State the preparation type.
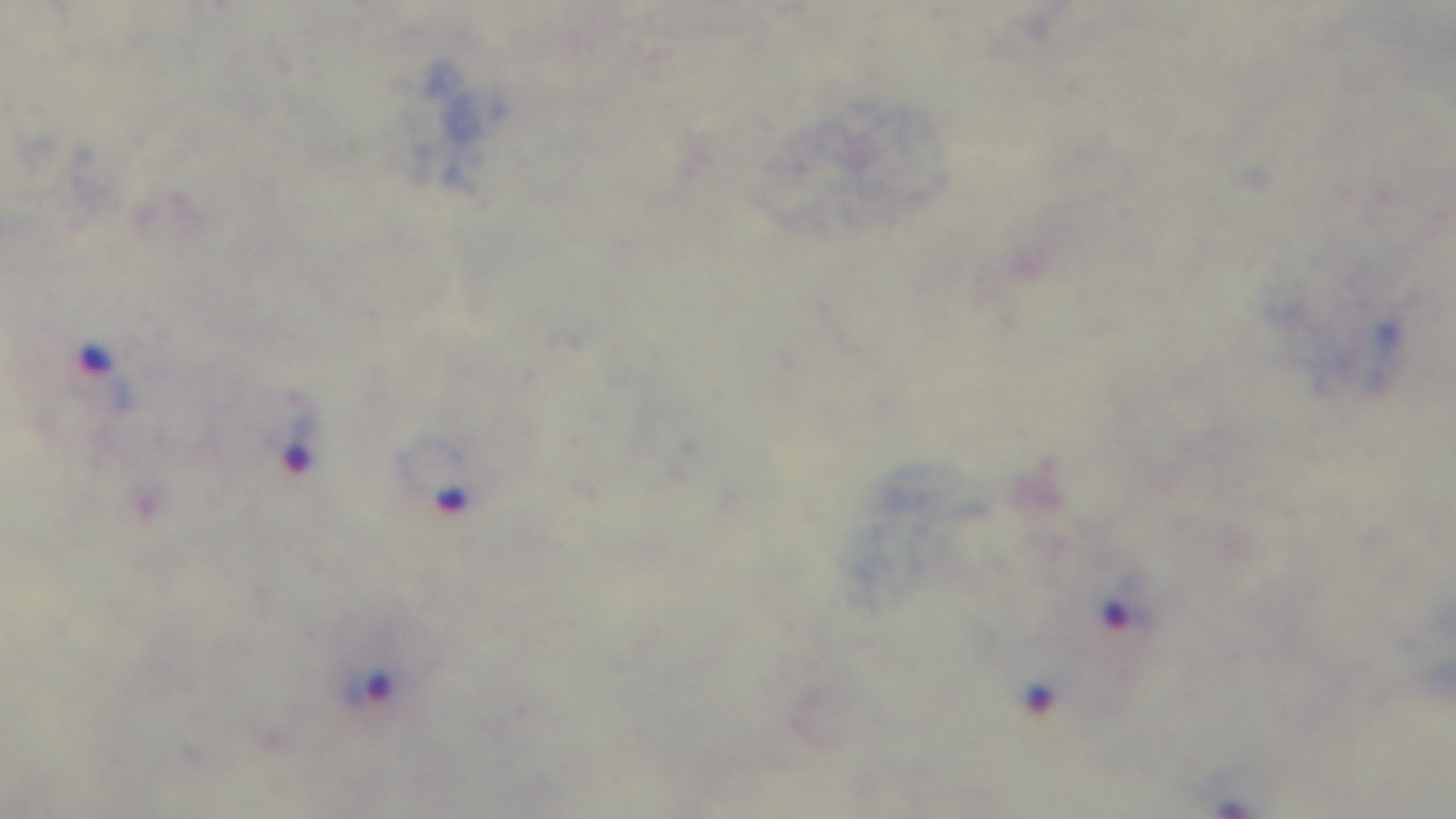
A thick smear.

field of view = single
capture = mounted 4K digital camera
objective = 100x oil immersion
modality = light microscopy
malaria status = positive
stain = Giemsa